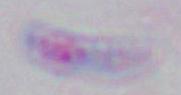
Summary:
  - Magnification: 1000x
  - Identification: Toxoplasma gondii
  - Modality: micrograph